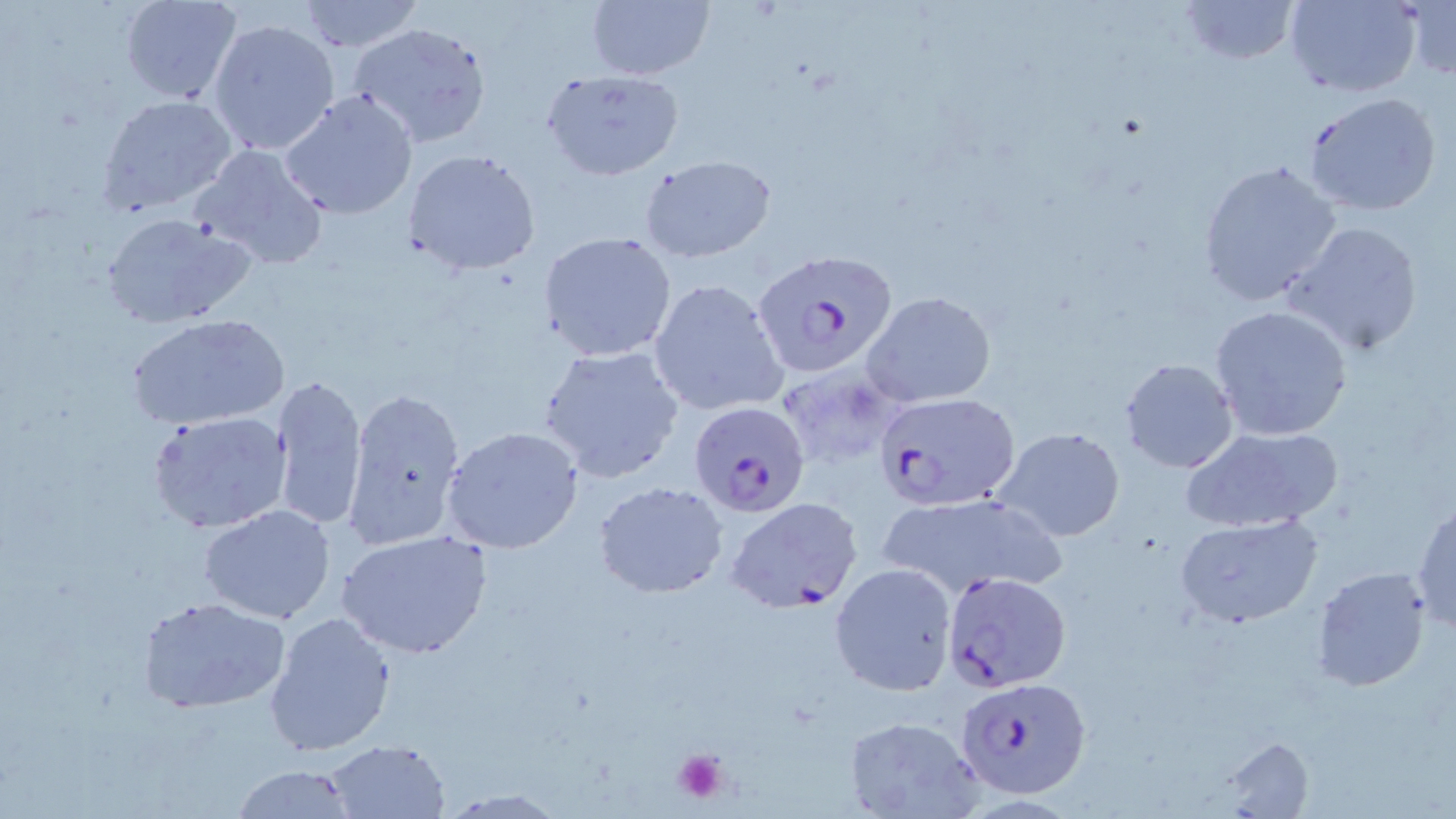
Summary:
  - Coordinate format: approximate bounding boxes as (x1,y1)-(x2,y2) corner pairs in pixels
  - Platelet locations: (670,747)-(730,806)
  - Plasmodium falciparum-infected red blood cell locations: (752,249)-(900,381), (871,391)-(1021,513), (687,400)-(811,517), (726,497)-(862,615), (943,569)-(1069,691), (957,675)-(1090,798)
  - Uninfected red blood cell locations: (119,0)-(242,106), (294,0)-(425,52), (583,0)-(714,83), (1177,0)-(1299,65), (1283,0)-(1421,98), (1403,0)-(1456,80), (208,17)-(340,158), (348,21)-(492,149), (541,70)-(684,180), (279,88)-(419,220), (1302,91)-(1444,217), (98,94)-(239,214), (189,142)-(331,272), (402,149)-(541,276), (641,155)-(777,264), (1196,160)-(1342,305), (99,209)-(261,329), (1283,220)-(1426,357), (538,231)-(678,361), (647,277)-(789,417), (864,290)-(996,407), (1208,304)-(1355,442), (129,313)-(290,431), (537,345)-(685,484), (1119,358)-(1239,473), (270,374)-(368,529), (341,385)-(467,550), (148,411)-(294,535), (1181,424)-(1344,534), (441,425)-(584,554), (993,425)-(1127,543), (592,481)-(731,599), (879,493)-(1061,600), (1412,500)-(1455,633), (199,505)-(336,624), (1174,513)-(1323,628), (336,530)-(491,660), (830,562)-(957,695), (1311,565)-(1433,691), (138,596)-(289,714), (263,610)-(398,757), (839,715)-(986,819), (1218,735)-(1316,816), (323,739)-(450,817), (230,764)-(360,818)
  - Slide-level diagnosis: Plasmodium falciparum
  - Image size: 1456×819 pixels
  - Preparation: thin blood smear
  - Field of view: one of a larger specimen
  - Magnification: 1000x
  - Stain: May-Grünwald-Giemsa
  - Modality: light microscopy